Locate and identify every blood parasite.
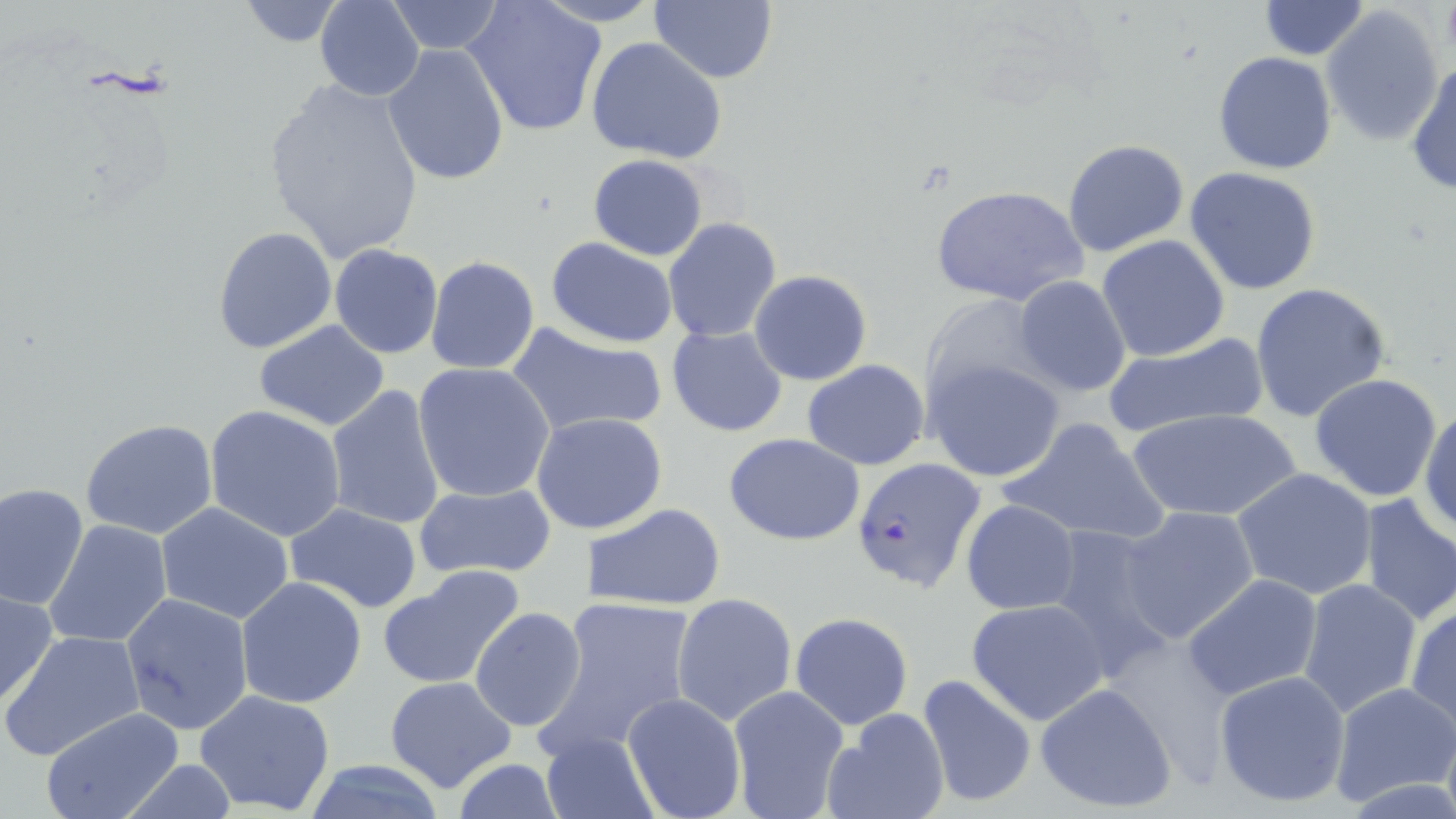

Approximate bounding boxes as [x1, y1, x2, y2] in pixels.
Plasmodium falciparum-infected red blood cells: [852, 456, 988, 595].
No Plasmodium ovale, Plasmodium malariae, Plasmodium vivax, Babesia divergens, or Trypanosoma brucei observed.

slide-level diagnosis = Plasmodium falciparum
image size = 1456×819 pixels
field of view = one of a larger specimen
magnification = 1000x
modality = optical microscopy
stain = May-Grünwald-Giemsa
preparation = thin blood smear
uninfected red blood cell locations = approximate bounding boxes as [x1, y1, x2, y2] in pixels: [315, 0, 426, 102], [465, 0, 608, 138], [650, 0, 778, 84], [1259, 0, 1369, 59], [385, 1, 506, 54], [237, 2, 347, 47], [1320, 5, 1444, 146], [587, 38, 726, 164], [382, 42, 511, 185], [1212, 51, 1338, 175], [1407, 57, 1456, 196], [259, 79, 427, 261], [1062, 138, 1191, 258], [588, 154, 709, 260], [1184, 165, 1322, 294], [929, 185, 1088, 308], [663, 217, 782, 340], [212, 225, 339, 355], [1096, 233, 1230, 363], [545, 237, 679, 347], [329, 244, 443, 358], [425, 256, 540, 374], [750, 270, 872, 385], [1012, 276, 1133, 397], [1249, 281, 1391, 423], [919, 292, 1053, 406], [250, 320, 393, 433], [507, 321, 668, 439], [666, 326, 788, 437], [1103, 333, 1269, 441], [925, 357, 1065, 482], [802, 359, 929, 469], [413, 362, 555, 503], [1308, 374, 1444, 503], [326, 384, 446, 530], [1419, 402, 1456, 537], [205, 404, 349, 541], [1129, 408, 1302, 523], [537, 414, 669, 534], [998, 417, 1169, 548], [80, 418, 218, 540], [724, 433, 866, 545], [1233, 468, 1378, 601], [412, 482, 556, 580], [0, 483, 89, 612], [1357, 493, 1456, 625], [961, 499, 1080, 614], [588, 501, 727, 611], [155, 503, 297, 624], [282, 503, 424, 615], [1119, 506, 1262, 643], [44, 519, 171, 649], [1042, 523, 1179, 674], [376, 565, 527, 691], [1182, 574, 1324, 701], [236, 577, 367, 707], [1296, 579, 1423, 720], [0, 587, 59, 712], [119, 591, 255, 737], [670, 592, 797, 725], [541, 596, 702, 753], [966, 599, 1110, 725], [1405, 602, 1456, 731], [470, 606, 586, 732], [790, 613, 914, 728], [3, 629, 144, 761], [1212, 669, 1352, 809], [917, 674, 1037, 807], [384, 675, 517, 794], [1034, 681, 1180, 814], [1329, 681, 1456, 808], [726, 685, 849, 819], [193, 688, 338, 813], [621, 692, 746, 819], [40, 707, 188, 819], [822, 708, 949, 819], [540, 731, 659, 818], [109, 759, 244, 816], [449, 760, 569, 819], [298, 761, 449, 817]